Assess this cell for malaria.
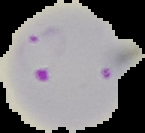
Parasitized.

Summary:
  - Image type: cell region segmented out of the field of view; surrounding area masked to black
  - Preparation: thin blood smear
  - Image size: 145×133 pixels